Identify the blood parasite species.
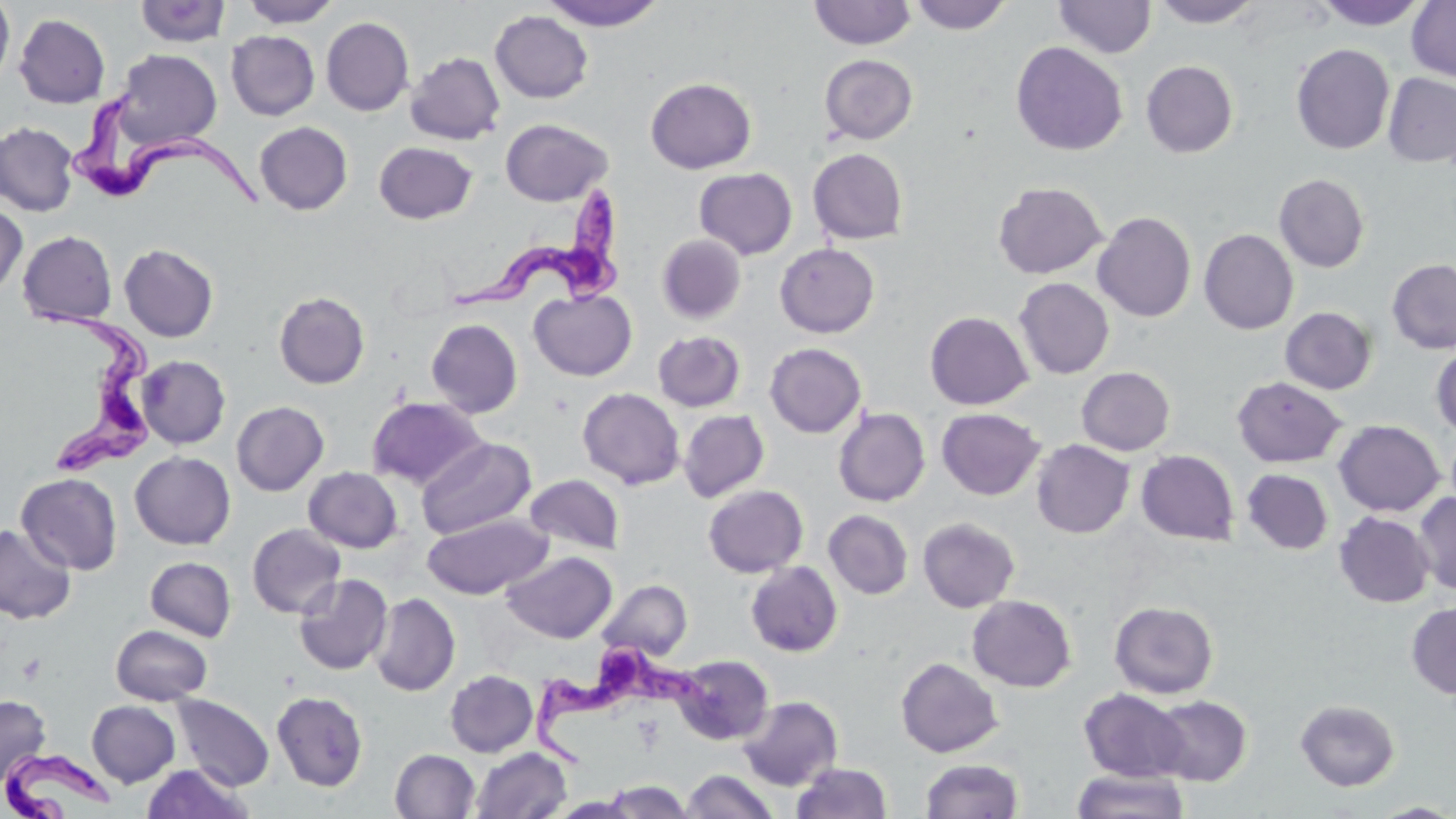
Trypanosoma brucei.

Approximate bounding boxes as (x1,y1)-(x2,y2) corner pairs in pixels. Platelet locations: (17,653)-(45,684). Trypanosoma brucei locations: (70,81)-(268,211), (449,183)-(623,322), (28,303)-(151,475), (530,629)-(719,770), (4,749)-(118,817). Uninfected red blood cell locations: (0,0)-(15,90), (240,0)-(341,28), (541,0)-(666,30), (909,0)-(1012,34), (1054,0)-(1155,59), (1151,0)-(1263,27), (1315,0)-(1427,30), (1407,0)-(1456,82), (134,1)-(231,48), (809,1)-(917,49), (490,11)-(593,104), (14,13)-(110,109), (321,17)-(414,116), (226,31)-(319,121), (1010,42)-(1128,156), (1291,43)-(1395,154), (113,49)-(221,150), (405,51)-(505,145), (819,54)-(918,144), (1141,60)-(1238,158), (1383,73)-(1456,168), (645,77)-(757,174), (501,118)-(613,206), (254,121)-(353,215), (0,122)-(78,216), (374,141)-(477,224), (808,148)-(908,244), (694,168)-(797,259), (1274,173)-(1370,273), (993,182)-(1107,279), (0,204)-(27,299), (1092,212)-(1196,322), (1199,229)-(1298,335), (18,231)-(117,326), (657,234)-(746,323), (119,243)-(219,342), (775,243)-(880,338), (1386,259)-(1456,354), (1014,277)-(1114,379), (529,289)-(637,381), (274,292)-(370,388), (1280,307)-(1377,394), (925,311)-(1033,410), (426,319)-(523,418), (653,330)-(746,412), (764,343)-(867,438), (1431,346)-(1456,438), (137,355)-(230,448), (1076,367)-(1175,455), (1232,376)-(1347,468), (577,388)-(685,490), (367,397)-(486,489), (231,401)-(329,496), (833,407)-(930,506), (936,408)-(1045,500), (679,410)-(769,502), (1333,420)-(1444,516), (416,437)-(536,539), (1032,439)-(1134,538), (1137,450)-(1239,545), (130,451)-(235,549), (303,467)-(403,553), (1242,468)-(1333,555), (16,472)-(122,575), (525,474)-(624,555), (703,484)-(808,577), (1412,492)-(1456,594), (823,510)-(913,599), (1334,512)-(1434,607), (422,513)-(552,599), (918,517)-(1020,612), (0,523)-(77,624), (247,523)-(345,619), (502,551)-(617,643), (145,556)-(236,641), (745,561)-(843,657), (293,573)-(393,675), (597,579)-(692,662), (370,593)-(460,696), (967,594)-(1076,692), (1109,601)-(1218,698), (1406,601)-(1456,700), (110,624)-(213,705), (672,655)-(773,745), (895,657)-(1003,758), (445,670)-(538,757), (1079,689)-(1190,782), (272,690)-(368,791), (172,694)-(274,790), (0,695)-(50,785), (738,695)-(842,790), (1151,695)-(1252,786), (1295,699)-(1400,791), (87,700)-(180,787), (470,747)-(572,819), (390,749)-(479,818), (920,759)-(1023,817), (792,762)-(892,819), (142,764)-(251,819), (1072,768)-(1189,819), (681,770)-(779,819), (602,778)-(697,819), (1369,801)-(1456,818). Thin blood smear. May-Grünwald-Giemsa-stained preparation. Optical microscopy. Captured at 1000x magnification. Image is 1456×819 pixels. Single field of view.